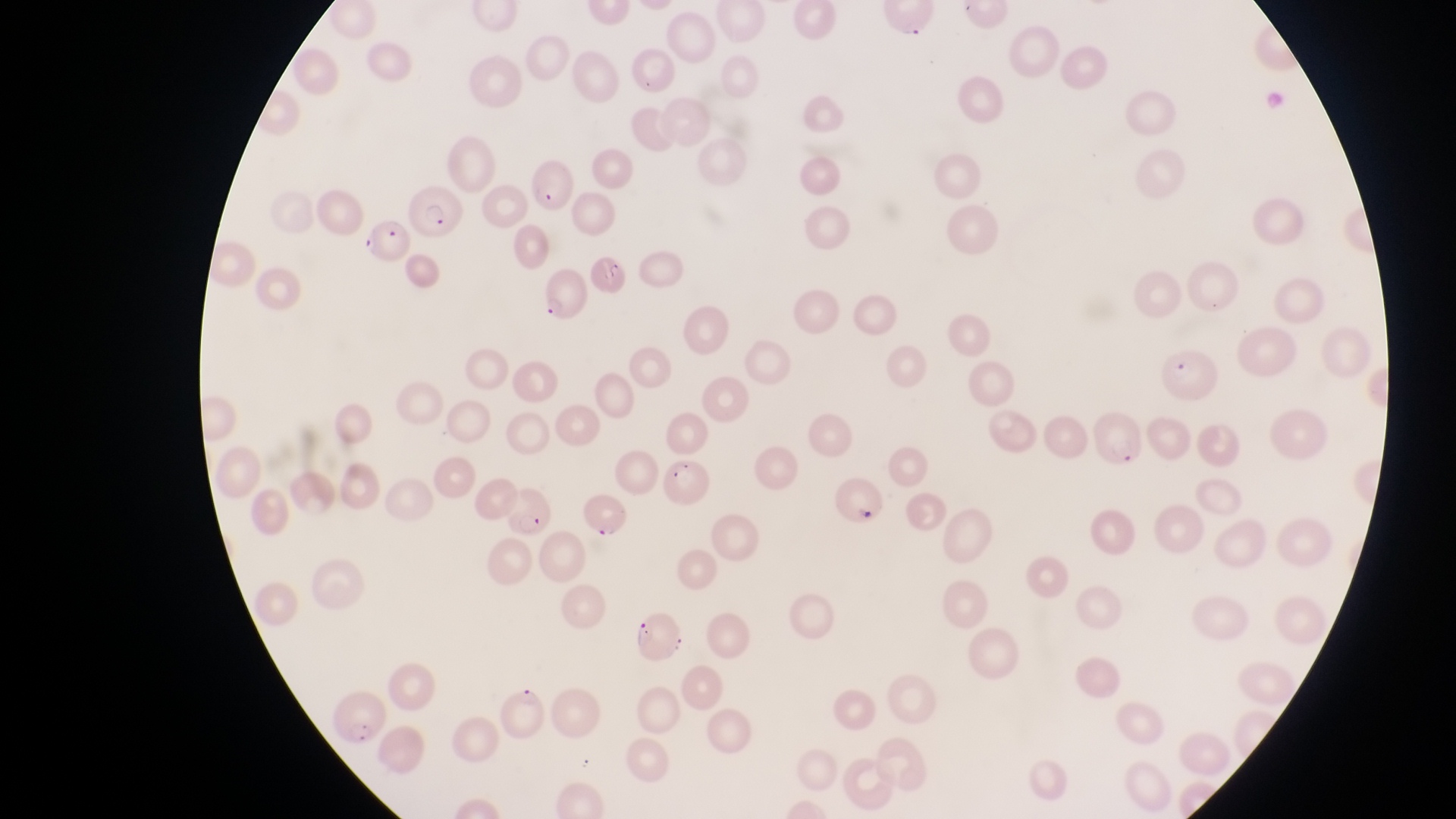
Approximate bounding boxes as {left, top, right, bottom} in pixels.
Summary:
  - Parasitised red blood cell locations: {406, 180, 462, 241}, {362, 219, 411, 265}, {536, 267, 586, 322}, {1160, 347, 1219, 400}, {833, 476, 885, 530}, {497, 488, 555, 541}, {582, 495, 631, 542}, {627, 610, 688, 663}, {330, 689, 385, 750}
  - Capture: smartphone photograph through the eyepiece of an Olympus CX-23 microscope
  - Field of view: single
  - Image size: 1456×819 pixels
  - Preparation: thin blood smear
  - Magnification: 1000x
  - Country: Uganda